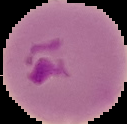

Malaria status: parasitized. Segmented cell region on a black background. Image is 127×124 pixels. From a thin blood smear.